Give the position of every leukocyte visible.
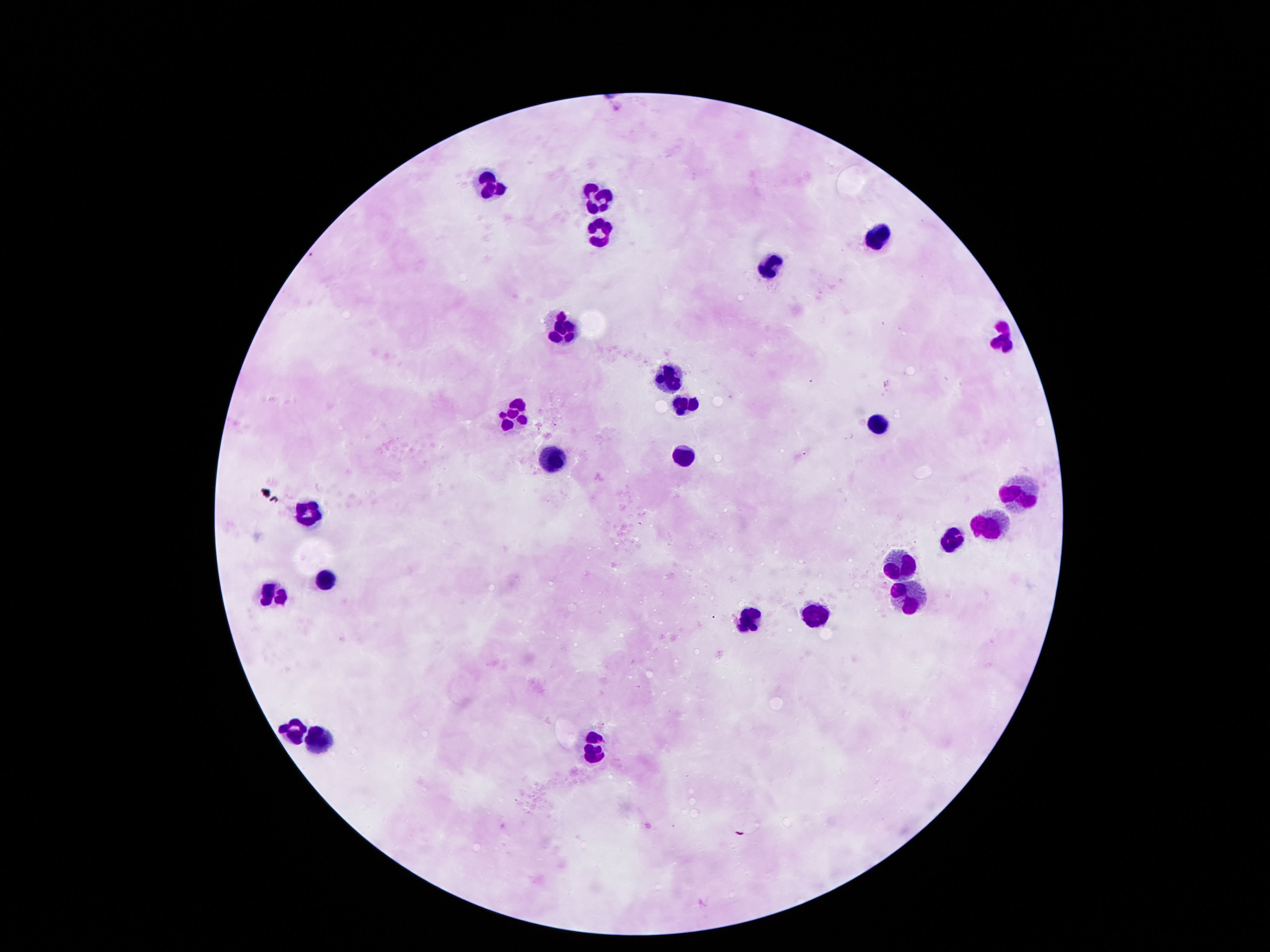
Approximate centers as (x, y) in pixels.
Leukocytes: (492, 192), (596, 196), (599, 237), (875, 237), (770, 269), (561, 329), (1001, 342), (669, 376), (683, 402), (516, 413), (880, 426), (684, 457), (550, 460), (1016, 498), (307, 510), (990, 522), (949, 541), (900, 562), (327, 576), (908, 593), (276, 598), (814, 613), (745, 619), (287, 729), (314, 738), (593, 749).

Summary:
  - Preparation: thick peripheral-blood smear
  - Capture: smartphone camera through the microscope eyepiece
  - Stain: Giemsa
  - Image size: 1270×952 pixels
  - Magnification: 100x
  - Field of view: one from this slide
  - Patient malaria status: not infected